Assess this cell for malaria.
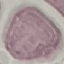
It is uninfected.

Summary:
  - Capture: smartphone through the microscope eyepiece
  - Stain: Giemsa
  - Image type: automatically extracted cell patch, resized to 64 × 64 pixels
  - Preparation: thin blood film